Outline each Plasmodium falciparum-infected red blood cell.
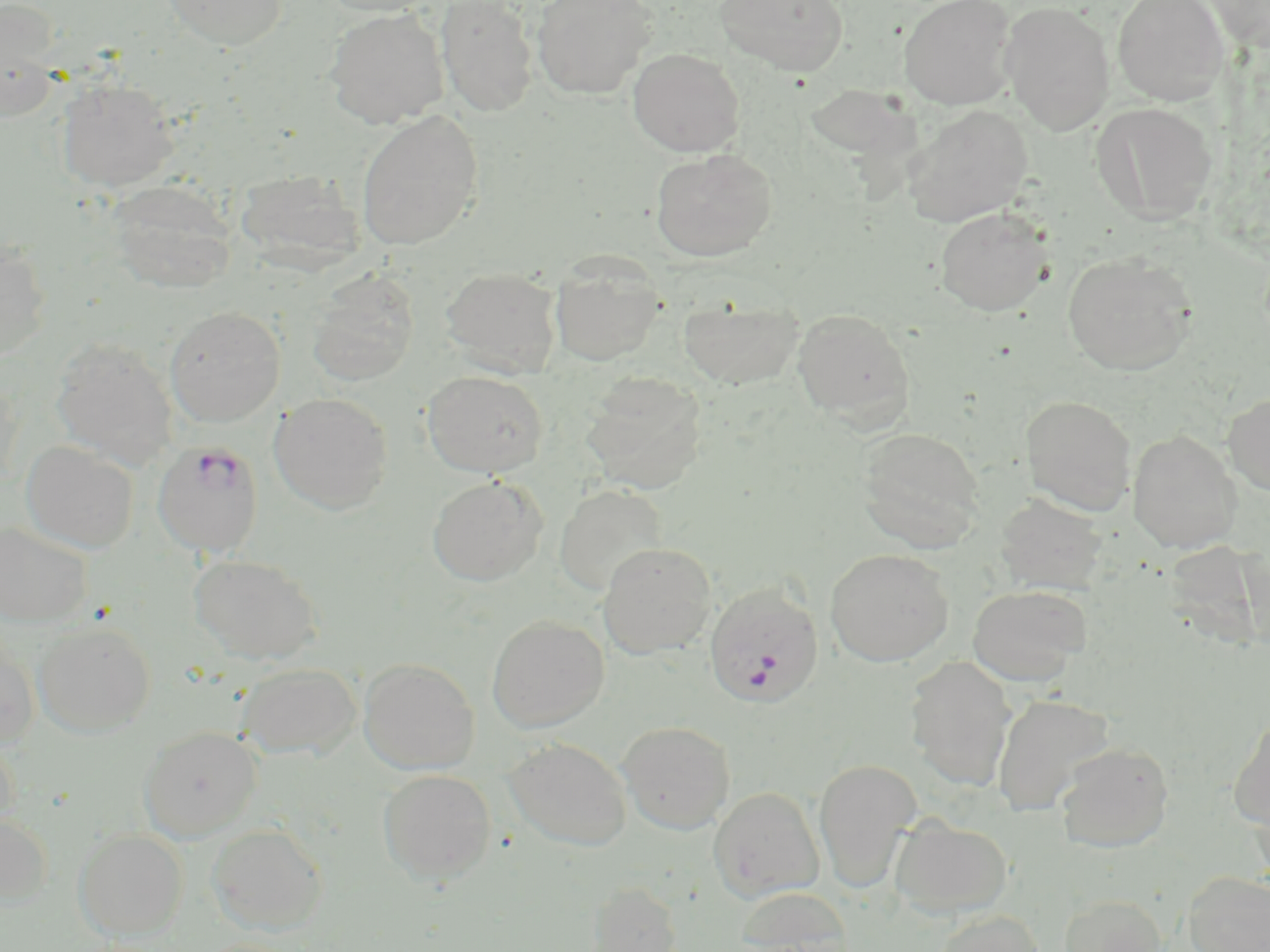

Approximate bounding boxes as named x1/y1/x2/y2 corners in pixels.
Plasmodium falciparum-infected red blood cells: (x1=153, y1=440, x2=264, y2=557), (x1=704, y1=583, x2=824, y2=708).

Uninfected red blood cell locations: (x1=159, y1=0, x2=289, y2=50), (x1=316, y1=0, x2=442, y2=17), (x1=436, y1=0, x2=539, y2=117), (x1=531, y1=0, x2=657, y2=100), (x1=715, y1=0, x2=849, y2=76), (x1=899, y1=0, x2=1018, y2=109), (x1=1112, y1=0, x2=1230, y2=105), (x1=1204, y1=0, x2=1270, y2=52), (x1=1000, y1=1, x2=1115, y2=135), (x1=0, y1=2, x2=63, y2=119), (x1=324, y1=9, x2=449, y2=128), (x1=628, y1=47, x2=745, y2=157), (x1=56, y1=78, x2=179, y2=192), (x1=792, y1=83, x2=931, y2=210), (x1=1091, y1=101, x2=1219, y2=224), (x1=902, y1=104, x2=1034, y2=228), (x1=356, y1=111, x2=483, y2=250), (x1=650, y1=148, x2=778, y2=261), (x1=243, y1=170, x2=372, y2=290), (x1=107, y1=180, x2=238, y2=294), (x1=934, y1=207, x2=1054, y2=316), (x1=0, y1=238, x2=52, y2=361), (x1=1062, y1=252, x2=1197, y2=376), (x1=550, y1=255, x2=665, y2=366), (x1=441, y1=266, x2=562, y2=378), (x1=306, y1=272, x2=418, y2=387), (x1=678, y1=295, x2=805, y2=389), (x1=164, y1=306, x2=285, y2=427), (x1=792, y1=308, x2=914, y2=426), (x1=50, y1=338, x2=179, y2=469), (x1=0, y1=370, x2=23, y2=490), (x1=422, y1=371, x2=549, y2=478), (x1=581, y1=373, x2=708, y2=494), (x1=269, y1=392, x2=393, y2=514), (x1=1223, y1=392, x2=1270, y2=496), (x1=1020, y1=395, x2=1137, y2=515), (x1=856, y1=426, x2=985, y2=551), (x1=1128, y1=429, x2=1241, y2=554), (x1=20, y1=440, x2=139, y2=553), (x1=427, y1=475, x2=547, y2=586), (x1=554, y1=484, x2=669, y2=596), (x1=995, y1=494, x2=1107, y2=594), (x1=0, y1=521, x2=93, y2=626), (x1=1171, y1=539, x2=1270, y2=649), (x1=598, y1=542, x2=717, y2=658), (x1=825, y1=548, x2=954, y2=667), (x1=189, y1=553, x2=323, y2=664), (x1=967, y1=583, x2=1091, y2=685), (x1=487, y1=615, x2=609, y2=732), (x1=33, y1=621, x2=156, y2=737), (x1=0, y1=637, x2=40, y2=748), (x1=904, y1=656, x2=1017, y2=790), (x1=359, y1=658, x2=479, y2=774), (x1=236, y1=662, x2=362, y2=759), (x1=992, y1=693, x2=1113, y2=816), (x1=1228, y1=715, x2=1270, y2=832), (x1=618, y1=720, x2=736, y2=834), (x1=139, y1=726, x2=262, y2=841), (x1=0, y1=734, x2=20, y2=837), (x1=504, y1=737, x2=632, y2=851), (x1=1056, y1=742, x2=1174, y2=852), (x1=813, y1=759, x2=921, y2=892), (x1=378, y1=769, x2=496, y2=884), (x1=708, y1=787, x2=825, y2=903), (x1=0, y1=811, x2=53, y2=907), (x1=890, y1=815, x2=1013, y2=918), (x1=207, y1=823, x2=328, y2=934), (x1=74, y1=829, x2=188, y2=940), (x1=1182, y1=870, x2=1270, y2=952), (x1=586, y1=880, x2=682, y2=952), (x1=735, y1=885, x2=853, y2=952), (x1=1059, y1=894, x2=1166, y2=952), (x1=935, y1=910, x2=1046, y2=952). Slide-level diagnosis: Plasmodium falciparum. 1000x magnification. Image is 1270×952 pixels. Single field of view. Thin blood film. May-Grünwald-Giemsa-stained preparation. Optical microscopy.